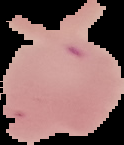
preparation = thin blood film
image type = segmented cell region with the area outside set to black
image size = 124×145 pixels
malaria status = parasitized